Assess this cell for malaria.
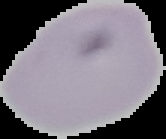
It is uninfected.

image type = segmented cell region with the area outside set to black
image size = 166×139 pixels
preparation = thin blood film